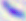

400x magnification. Toxoplasma gondii is shown. Micrograph.